Give the preparation type.
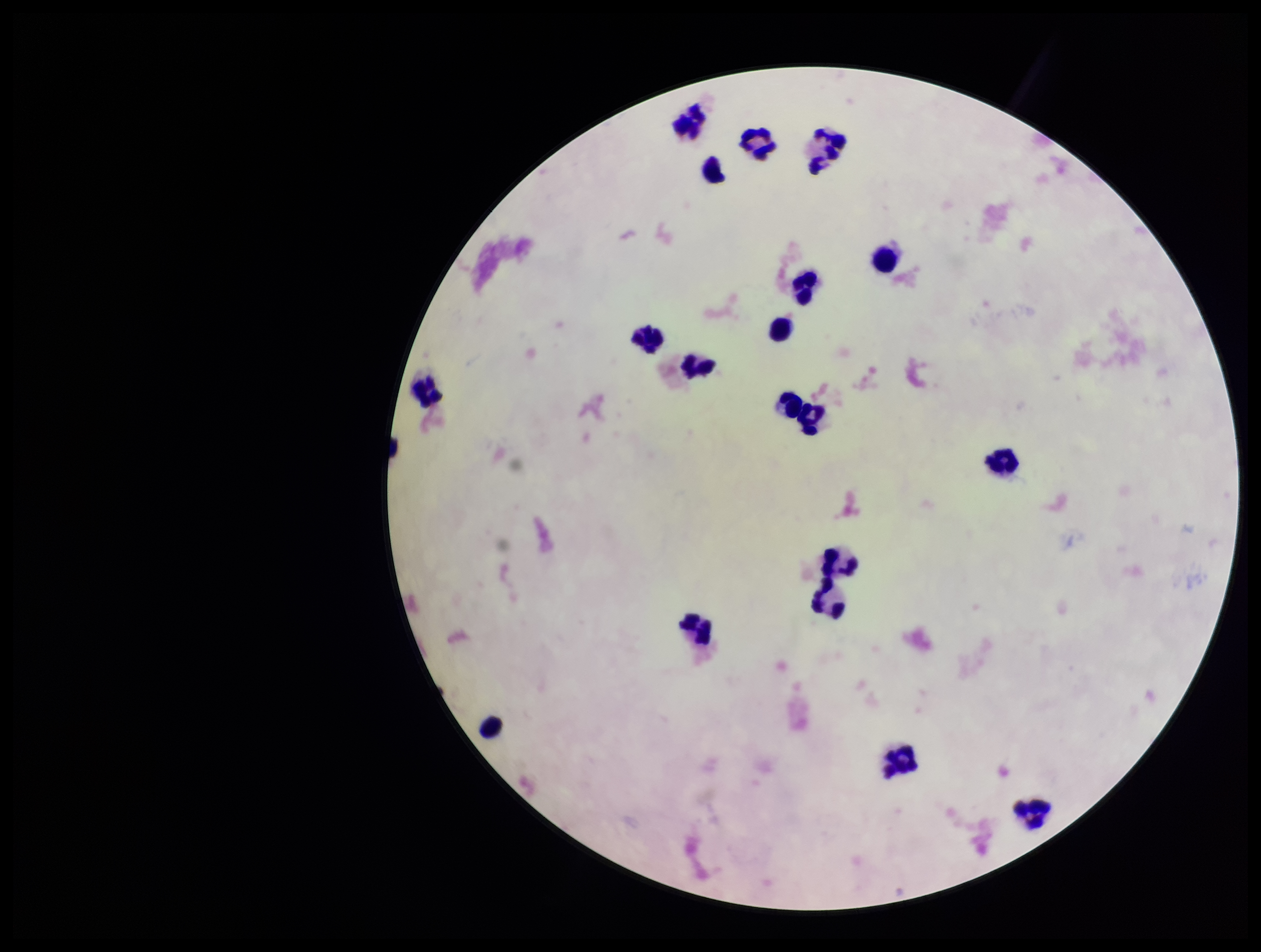
A thick smear.

Stained with Giemsa. Parasite count: 0. One field from this slide. Patient malaria status: negative. Smartphone photograph taken through the eyepiece of a microscope. Image is 1261×952 pixels. Leukocyte count: 19. Plasmodium parasites: none detected.